Identify the blood parasite species.
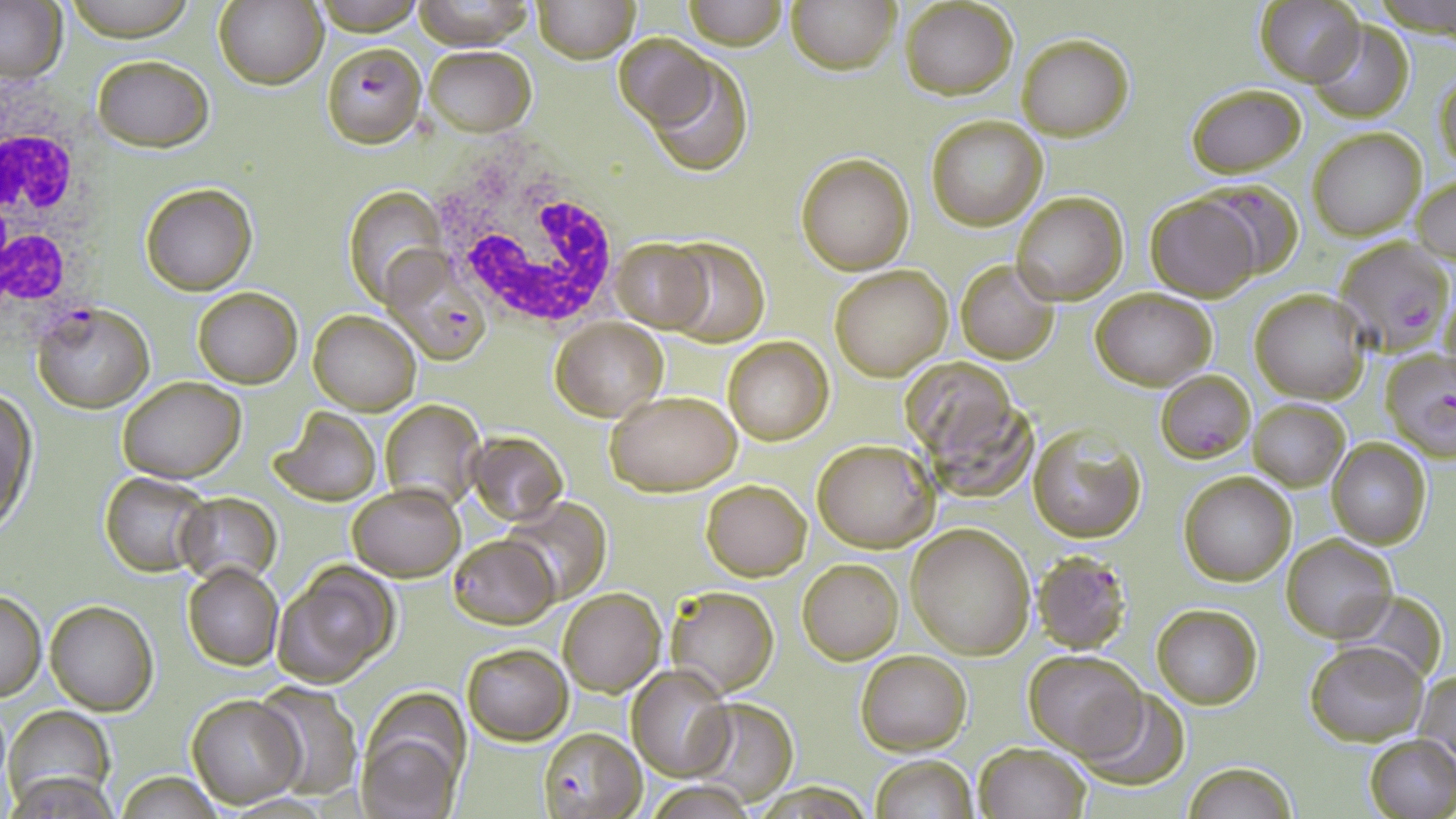

Plasmodium falciparum.

Approximate bounding boxes as (x1, y1, x2, y2) in pixels. Plasmodium falciparum-infected red blood cell locations: (321, 41, 428, 148), (1196, 183, 1304, 277), (1331, 236, 1453, 353), (383, 250, 492, 366), (33, 303, 152, 412), (1379, 350, 1456, 458), (1155, 370, 1255, 462), (1032, 552, 1134, 658), (537, 727, 645, 819). White blood cell locations: (0, 77, 100, 330), (425, 147, 626, 339). Uninfected red blood cell locations: (61, 0, 199, 40), (314, 0, 428, 33), (533, 0, 639, 63), (682, 0, 786, 50), (788, 0, 899, 75), (899, 0, 1017, 99), (0, 1, 67, 85), (214, 1, 327, 89), (410, 2, 536, 49), (1255, 2, 1363, 85), (1307, 21, 1413, 123), (612, 31, 721, 133), (1016, 34, 1133, 141), (422, 45, 537, 135), (644, 54, 754, 177), (93, 56, 214, 149), (1433, 73, 1456, 179), (1186, 82, 1306, 179), (925, 115, 1048, 230), (1308, 129, 1426, 241), (795, 153, 915, 274), (1412, 175, 1456, 267), (139, 182, 257, 296), (343, 185, 443, 307), (1012, 192, 1128, 304), (1147, 197, 1259, 301), (659, 236, 770, 345), (610, 239, 712, 331), (956, 260, 1060, 365), (829, 265, 953, 381), (192, 286, 302, 389), (1090, 287, 1217, 390), (1252, 289, 1369, 402), (309, 310, 420, 414), (551, 318, 667, 421), (723, 336, 833, 445), (903, 354, 1018, 464), (117, 376, 246, 484), (604, 390, 742, 495), (1, 393, 35, 533), (1248, 399, 1350, 490), (380, 400, 485, 509), (930, 402, 1045, 500), (268, 407, 380, 507), (1029, 429, 1146, 543), (465, 431, 567, 523), (812, 438, 938, 552), (1327, 439, 1432, 548), (100, 471, 212, 577), (1180, 471, 1295, 587), (701, 479, 810, 581), (348, 483, 465, 581), (174, 493, 281, 586), (503, 497, 609, 604), (906, 522, 1037, 660), (1281, 534, 1397, 642), (447, 535, 554, 627), (797, 557, 903, 664), (183, 563, 282, 670), (274, 564, 400, 686), (557, 586, 665, 697), (666, 586, 779, 697), (0, 589, 46, 701), (1340, 589, 1450, 686), (46, 602, 156, 715), (1152, 605, 1260, 709), (1307, 641, 1429, 747), (462, 643, 572, 744), (855, 648, 973, 756), (1024, 650, 1146, 758), (628, 666, 733, 780), (1415, 670, 1456, 773), (253, 680, 364, 800), (1078, 688, 1190, 789), (188, 693, 304, 807), (691, 697, 797, 804), (6, 706, 115, 809), (357, 731, 460, 819), (1364, 736, 1456, 819), (973, 742, 1090, 819), (869, 754, 978, 819), (1183, 763, 1297, 818), (8, 768, 117, 817), (115, 772, 225, 818), (649, 782, 754, 817). May-Grünwald-Giemsa stain. Captured at 1000x magnification. Single field of view. Image is 1456×819 pixels. Optical microscopy. Thin blood smear.